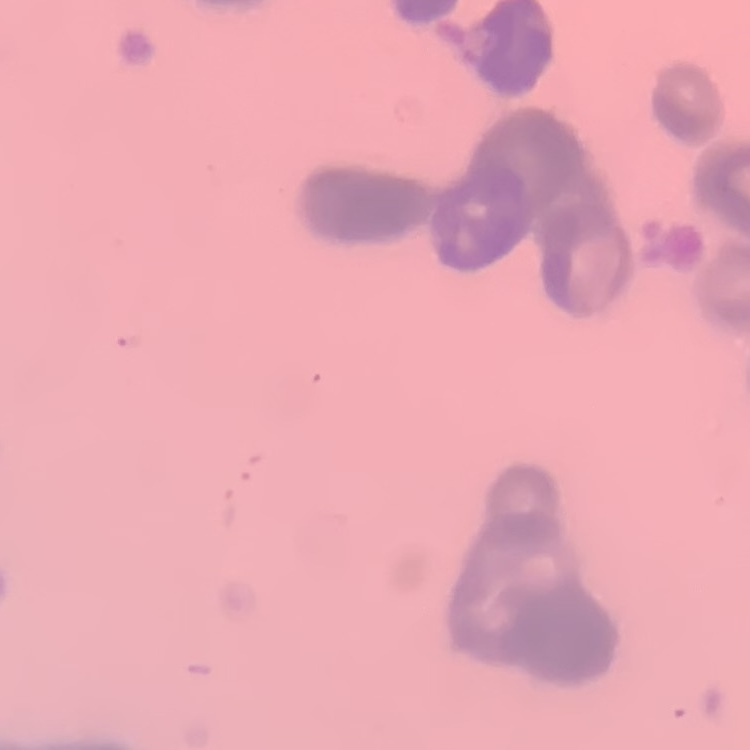

red blood cell morphology = rouleaux formation
stain = Field's or Giemsa
image type = square crop of a larger photomicrograph
preparation = thin peripheral smear